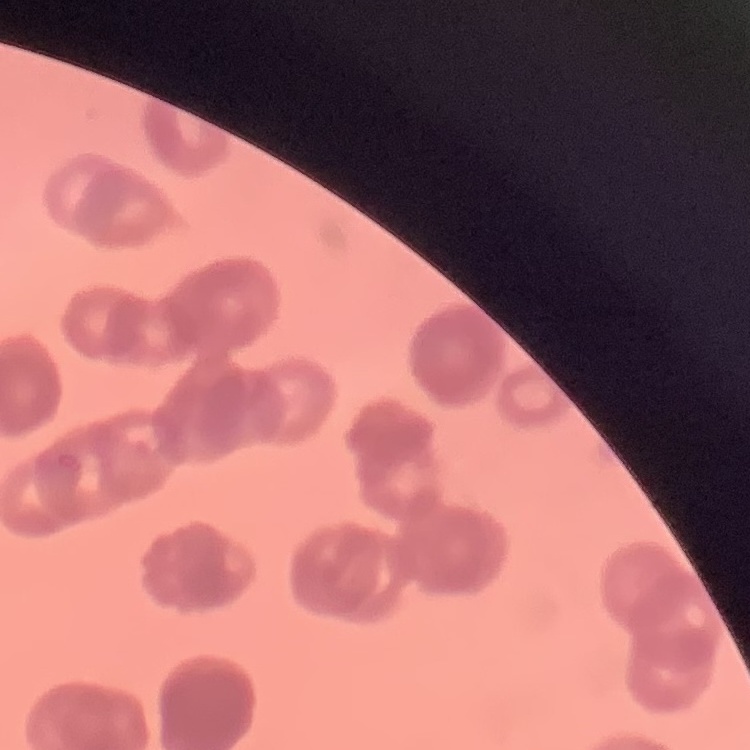
The erythrocytes show rouleaux formation. Thin peripheral smear. Square crop of a larger photomicrograph. Field's or Giemsa stain.